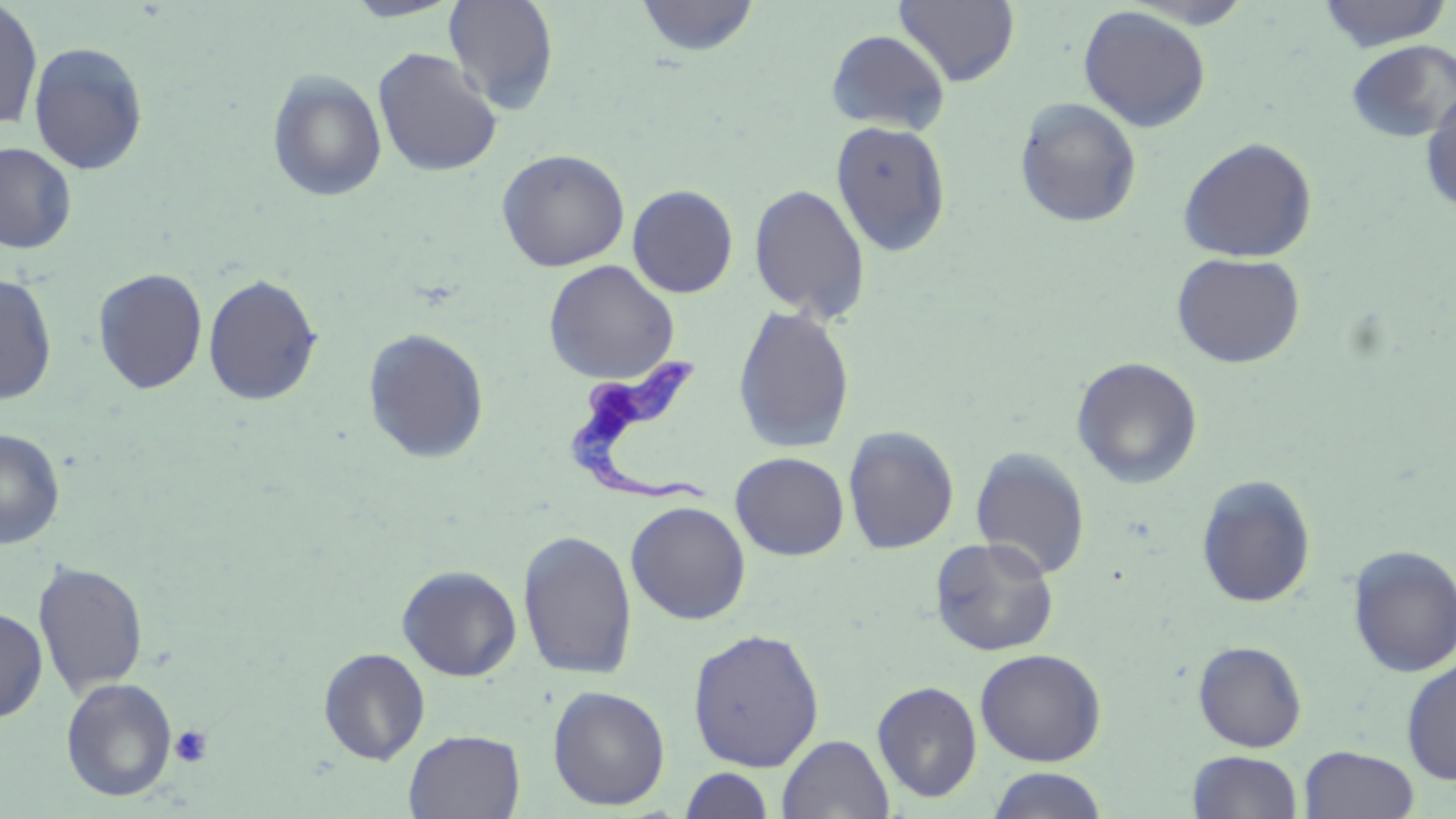
Summary:
  - Coordinate format: approximate bounding boxes as [x1, y1, x2, y2] in pixels
  - Uninfected red blood cell locations: [342, 0, 464, 22], [443, 0, 560, 113], [635, 0, 759, 57], [894, 0, 1020, 87], [1125, 0, 1256, 29], [1316, 0, 1453, 52], [0, 2, 42, 130], [1078, 5, 1211, 132], [825, 29, 950, 135], [1345, 39, 1456, 143], [27, 41, 149, 175], [372, 48, 503, 178], [267, 70, 388, 203], [1420, 91, 1456, 216], [1014, 97, 1142, 228], [830, 120, 952, 256], [1178, 136, 1317, 263], [0, 143, 77, 253], [496, 149, 630, 272], [748, 183, 871, 324], [627, 185, 739, 299], [1171, 252, 1306, 369], [544, 260, 679, 383], [92, 267, 208, 395], [0, 273, 57, 404], [202, 274, 323, 406], [732, 305, 856, 453], [362, 327, 490, 464], [1071, 356, 1203, 489], [843, 425, 959, 554], [0, 428, 65, 549], [970, 447, 1090, 579], [730, 452, 849, 560], [1195, 474, 1317, 609], [625, 501, 751, 625], [518, 529, 638, 681], [930, 536, 1060, 656], [1348, 545, 1456, 677], [33, 560, 149, 697], [397, 565, 522, 681], [0, 607, 48, 723], [687, 627, 825, 772], [1193, 640, 1307, 752], [317, 648, 430, 764], [974, 648, 1107, 766], [1401, 658, 1456, 784], [60, 677, 178, 801], [872, 680, 982, 803], [547, 685, 670, 811], [404, 730, 525, 818], [777, 734, 894, 818], [1299, 745, 1419, 819], [1187, 750, 1302, 819], [680, 767, 775, 818], [985, 767, 1111, 819]
  - Trypanosoma brucei locations: [564, 355, 719, 504]
  - Platelet locations: [169, 725, 213, 768]
  - Slide-level diagnosis: Trypanosoma brucei
  - Stain: May-Grünwald-Giemsa
  - Preparation: thin blood film
  - Modality: light microscopy
  - Magnification: 1000x
  - Field of view: single
  - Image size: 1456×819 pixels